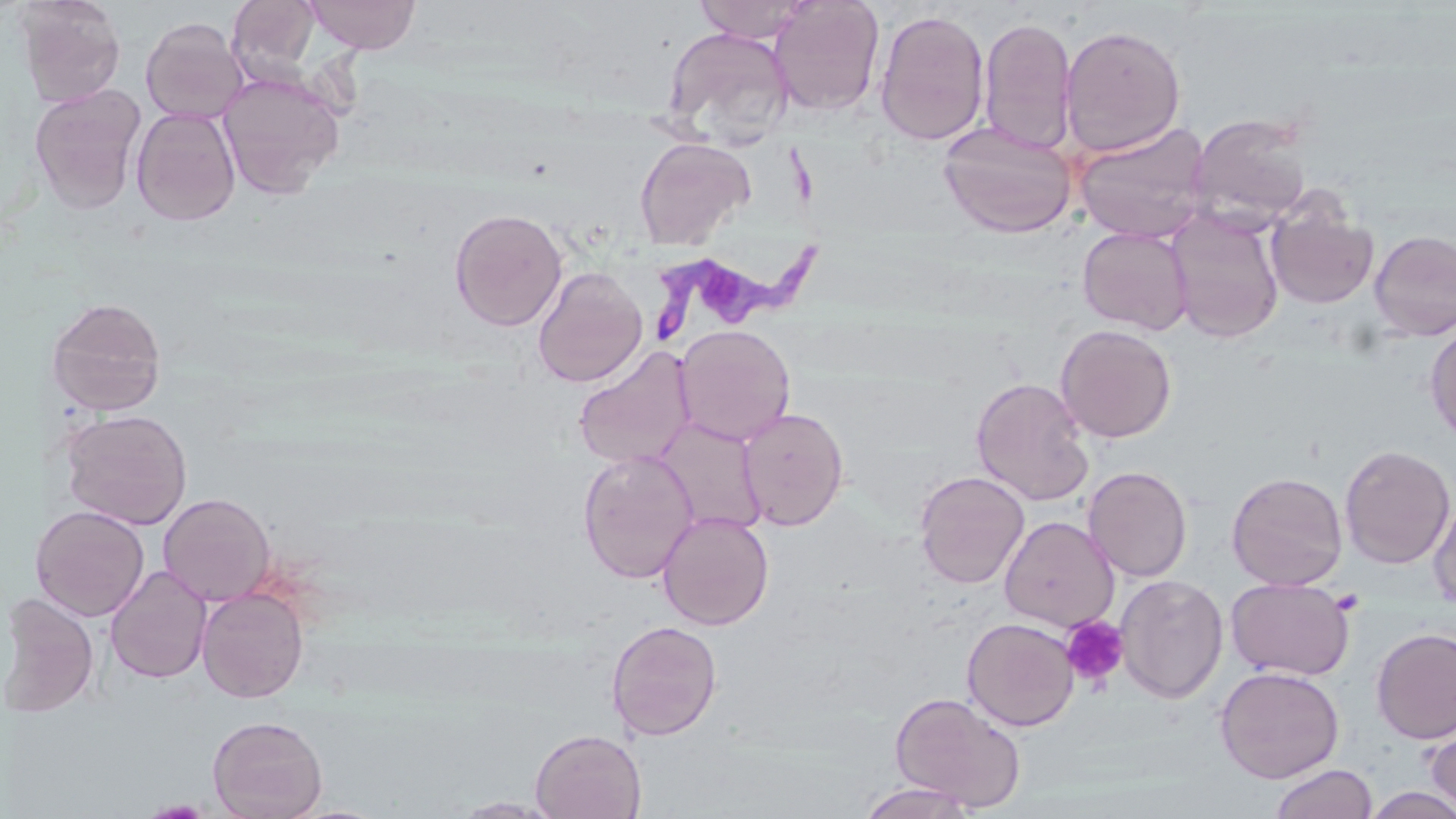

Approximate bounding boxes as (x1,y1)-(x2,y2) corner pairs in pixels. Trypanosoma brucei locations: (649,149)-(822,347). Uninfected red blood cell locations: (16,0)-(126,108), (226,0)-(324,86), (303,0)-(422,54), (694,0)-(815,42), (768,0)-(885,117), (874,9)-(990,146), (140,17)-(248,124), (978,17)-(1077,155), (1059,23)-(1187,156), (662,26)-(795,148), (217,71)-(345,199), (29,85)-(146,214), (131,106)-(241,226), (1187,111)-(1315,226), (938,120)-(1077,238), (1073,120)-(1212,243), (634,136)-(755,251), (1267,203)-(1378,309), (448,207)-(568,331), (1167,209)-(1284,344), (1077,226)-(1194,336), (1369,230)-(1456,340), (532,266)-(648,387), (46,297)-(167,416), (1425,322)-(1456,444), (675,324)-(796,446), (1055,324)-(1177,443), (573,347)-(696,470), (970,378)-(1095,507), (739,407)-(849,530), (60,408)-(193,529), (655,417)-(768,536), (1339,444)-(1455,569), (578,450)-(699,583), (1082,465)-(1193,582), (914,470)-(1030,589), (1226,471)-(1349,591), (158,492)-(276,606), (1428,494)-(1456,609), (39,505)-(150,621), (657,511)-(774,630), (999,516)-(1120,632), (106,565)-(212,684), (1115,574)-(1228,703), (1226,578)-(1355,681), (197,586)-(309,703), (5,592)-(100,718), (961,617)-(1079,731), (606,620)-(722,741), (1371,626)-(1456,744), (1215,665)-(1345,783), (890,691)-(1026,811), (207,715)-(328,818), (1424,721)-(1456,814), (530,729)-(647,819), (1270,763)-(1379,819), (858,782)-(980,819), (1360,786)-(1456,819), (450,797)-(561,818). Platelet locations: (1060,616)-(1130,689). Slide-level diagnosis: Trypanosoma brucei. Thin blood smear. 1000x magnification. Image is 1456×819 pixels. One field of a larger specimen. Optical microscopy. May-Grünwald-Giemsa-stained preparation.